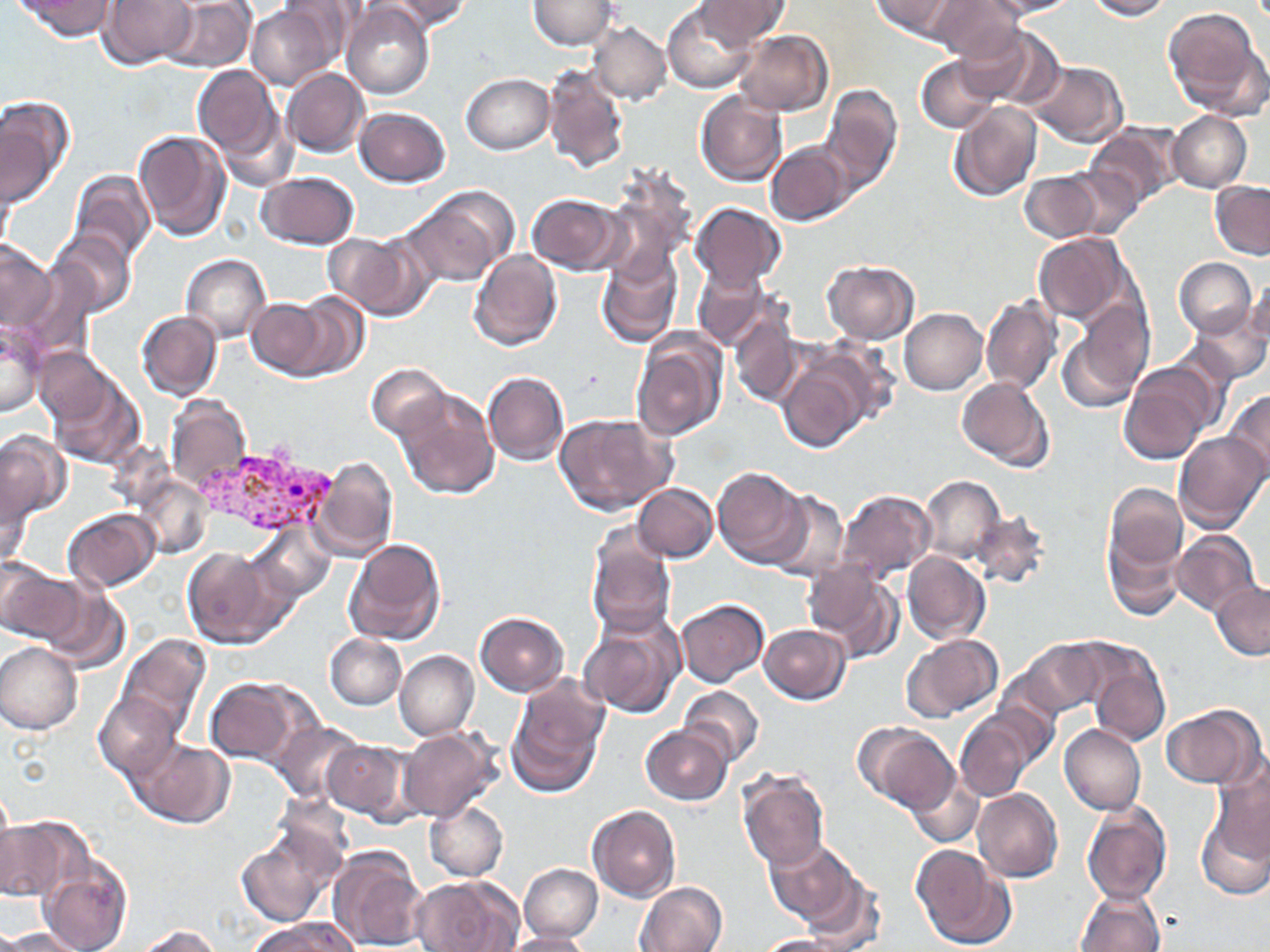
Summary:
  - Coordinate format: approximate bounding boxes as named x1/y1/x2/y2 corners in pixels
  - Plasmodium vivax-infected red blood cell locations: (x1=198, y1=441, x2=335, y2=538)
  - Uninfected red blood cell locations: (x1=16, y1=0, x2=116, y2=41), (x1=97, y1=0, x2=198, y2=68), (x1=159, y1=0, x2=256, y2=72), (x1=871, y1=0, x2=964, y2=39), (x1=931, y1=0, x2=1025, y2=62), (x1=986, y1=0, x2=1080, y2=18), (x1=1087, y1=0, x2=1170, y2=20), (x1=275, y1=1, x2=361, y2=71), (x1=381, y1=1, x2=470, y2=34), (x1=528, y1=1, x2=617, y2=50), (x1=695, y1=1, x2=787, y2=47), (x1=663, y1=3, x2=758, y2=92), (x1=342, y1=4, x2=432, y2=100), (x1=246, y1=5, x2=336, y2=90), (x1=1162, y1=7, x2=1266, y2=117), (x1=589, y1=22, x2=671, y2=105), (x1=957, y1=26, x2=1059, y2=107), (x1=734, y1=30, x2=832, y2=117), (x1=916, y1=56, x2=999, y2=133), (x1=1025, y1=61, x2=1128, y2=147), (x1=540, y1=62, x2=629, y2=173), (x1=193, y1=65, x2=286, y2=167), (x1=283, y1=68, x2=369, y2=157), (x1=460, y1=74, x2=553, y2=154), (x1=822, y1=86, x2=902, y2=192), (x1=695, y1=90, x2=786, y2=186), (x1=151, y1=91, x2=260, y2=225), (x1=0, y1=98, x2=73, y2=204), (x1=947, y1=102, x2=1042, y2=203), (x1=355, y1=107, x2=450, y2=186), (x1=1168, y1=111, x2=1251, y2=192), (x1=1085, y1=124, x2=1181, y2=208), (x1=133, y1=129, x2=231, y2=241), (x1=767, y1=142, x2=855, y2=225), (x1=1056, y1=168, x2=1143, y2=240), (x1=598, y1=169, x2=696, y2=286), (x1=1021, y1=169, x2=1106, y2=243), (x1=1, y1=170, x2=16, y2=258), (x1=69, y1=170, x2=155, y2=264), (x1=257, y1=171, x2=359, y2=249), (x1=1210, y1=182, x2=1269, y2=259), (x1=404, y1=187, x2=515, y2=287), (x1=526, y1=193, x2=625, y2=275), (x1=689, y1=203, x2=785, y2=289), (x1=48, y1=228, x2=137, y2=318), (x1=326, y1=231, x2=429, y2=319), (x1=1034, y1=234, x2=1133, y2=326), (x1=0, y1=239, x2=56, y2=333), (x1=7, y1=247, x2=89, y2=351), (x1=469, y1=248, x2=562, y2=350), (x1=181, y1=253, x2=271, y2=343), (x1=596, y1=254, x2=681, y2=349), (x1=1174, y1=258, x2=1256, y2=337), (x1=821, y1=261, x2=920, y2=343), (x1=693, y1=266, x2=775, y2=349), (x1=1244, y1=275, x2=1270, y2=347), (x1=282, y1=292, x2=372, y2=381), (x1=981, y1=296, x2=1063, y2=396), (x1=244, y1=297, x2=336, y2=379), (x1=1059, y1=306, x2=1151, y2=412), (x1=899, y1=308, x2=988, y2=395), (x1=1184, y1=308, x2=1268, y2=384), (x1=728, y1=310, x2=801, y2=407), (x1=136, y1=311, x2=222, y2=399), (x1=0, y1=324, x2=46, y2=417), (x1=632, y1=330, x2=728, y2=442), (x1=33, y1=348, x2=111, y2=425), (x1=776, y1=349, x2=881, y2=453), (x1=1120, y1=362, x2=1217, y2=466), (x1=367, y1=363, x2=449, y2=441), (x1=46, y1=367, x2=145, y2=469), (x1=482, y1=370, x2=569, y2=465), (x1=956, y1=376, x2=1054, y2=472), (x1=392, y1=387, x2=499, y2=500), (x1=1225, y1=391, x2=1270, y2=481), (x1=164, y1=395, x2=250, y2=493), (x1=554, y1=414, x2=674, y2=517), (x1=0, y1=432, x2=68, y2=526), (x1=1173, y1=432, x2=1268, y2=533), (x1=312, y1=457, x2=398, y2=562), (x1=711, y1=465, x2=810, y2=568), (x1=0, y1=469, x2=33, y2=566), (x1=133, y1=474, x2=212, y2=559), (x1=918, y1=475, x2=1005, y2=564), (x1=633, y1=483, x2=717, y2=562), (x1=1105, y1=484, x2=1187, y2=571), (x1=765, y1=490, x2=850, y2=581), (x1=835, y1=490, x2=936, y2=582), (x1=63, y1=509, x2=160, y2=590), (x1=971, y1=510, x2=1050, y2=590), (x1=926, y1=519, x2=1042, y2=605), (x1=248, y1=522, x2=336, y2=604), (x1=1170, y1=530, x2=1261, y2=616), (x1=585, y1=531, x2=677, y2=638), (x1=1104, y1=531, x2=1184, y2=621), (x1=341, y1=537, x2=447, y2=647), (x1=182, y1=547, x2=286, y2=650), (x1=902, y1=552, x2=991, y2=645), (x1=0, y1=560, x2=81, y2=645), (x1=801, y1=561, x2=905, y2=662), (x1=38, y1=581, x2=131, y2=673), (x1=1211, y1=584, x2=1270, y2=660), (x1=674, y1=598, x2=770, y2=687), (x1=580, y1=610, x2=686, y2=717), (x1=474, y1=613, x2=568, y2=695), (x1=759, y1=624, x2=850, y2=703), (x1=325, y1=633, x2=407, y2=710), (x1=116, y1=634, x2=211, y2=739), (x1=900, y1=634, x2=1003, y2=723), (x1=1019, y1=640, x2=1106, y2=718), (x1=1078, y1=640, x2=1171, y2=746), (x1=323, y1=642, x2=477, y2=721), (x1=0, y1=643, x2=83, y2=734), (x1=395, y1=650, x2=479, y2=740), (x1=506, y1=677, x2=609, y2=796), (x1=207, y1=678, x2=306, y2=766), (x1=678, y1=685, x2=765, y2=767), (x1=93, y1=693, x2=183, y2=780), (x1=1162, y1=704, x2=1266, y2=788), (x1=955, y1=714, x2=1031, y2=803), (x1=270, y1=720, x2=363, y2=803), (x1=855, y1=723, x2=958, y2=811), (x1=1058, y1=723, x2=1146, y2=814), (x1=640, y1=725, x2=733, y2=805), (x1=398, y1=726, x2=503, y2=822), (x1=131, y1=738, x2=235, y2=828), (x1=322, y1=738, x2=414, y2=821), (x1=1209, y1=763, x2=1270, y2=862), (x1=738, y1=771, x2=830, y2=871), (x1=906, y1=774, x2=984, y2=847), (x1=974, y1=789, x2=1063, y2=882), (x1=424, y1=799, x2=508, y2=882), (x1=1082, y1=802, x2=1171, y2=906), (x1=587, y1=806, x2=680, y2=902), (x1=1197, y1=812, x2=1270, y2=901), (x1=0, y1=817, x2=83, y2=906), (x1=236, y1=830, x2=339, y2=927), (x1=766, y1=840, x2=860, y2=929), (x1=325, y1=845, x2=428, y2=952), (x1=910, y1=845, x2=1012, y2=950), (x1=36, y1=855, x2=132, y2=952), (x1=519, y1=863, x2=602, y2=942), (x1=794, y1=871, x2=885, y2=950), (x1=412, y1=875, x2=522, y2=952), (x1=635, y1=881, x2=727, y2=952), (x1=1075, y1=889, x2=1166, y2=952), (x1=256, y1=918, x2=359, y2=952), (x1=137, y1=924, x2=222, y2=952), (x1=1, y1=927, x2=86, y2=950), (x1=499, y1=931, x2=594, y2=952), (x1=757, y1=935, x2=851, y2=952)
  - Slide-level diagnosis: Plasmodium vivax
  - Image size: 1270×952 pixels
  - Magnification: 1000x
  - Stain: May-Grünwald-Giemsa
  - Modality: light microscopy
  - Field of view: one of a larger specimen
  - Preparation: thin blood film